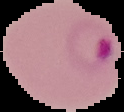
Summary:
  - Result: malaria parasites identified
  - Image type: segmented cell region with the area outside set to black
  - Preparation: thin blood film
  - Image size: 124×112 pixels